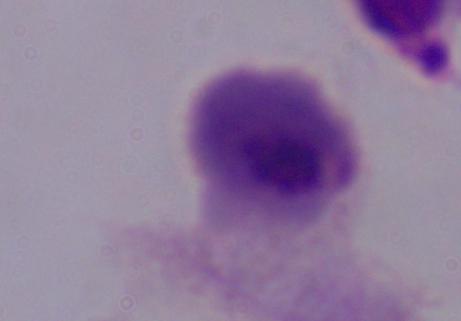
Summary:
  - Magnification: 1000x
  - Modality: micrograph
  - Identification: trichomonad